Locate platelets.
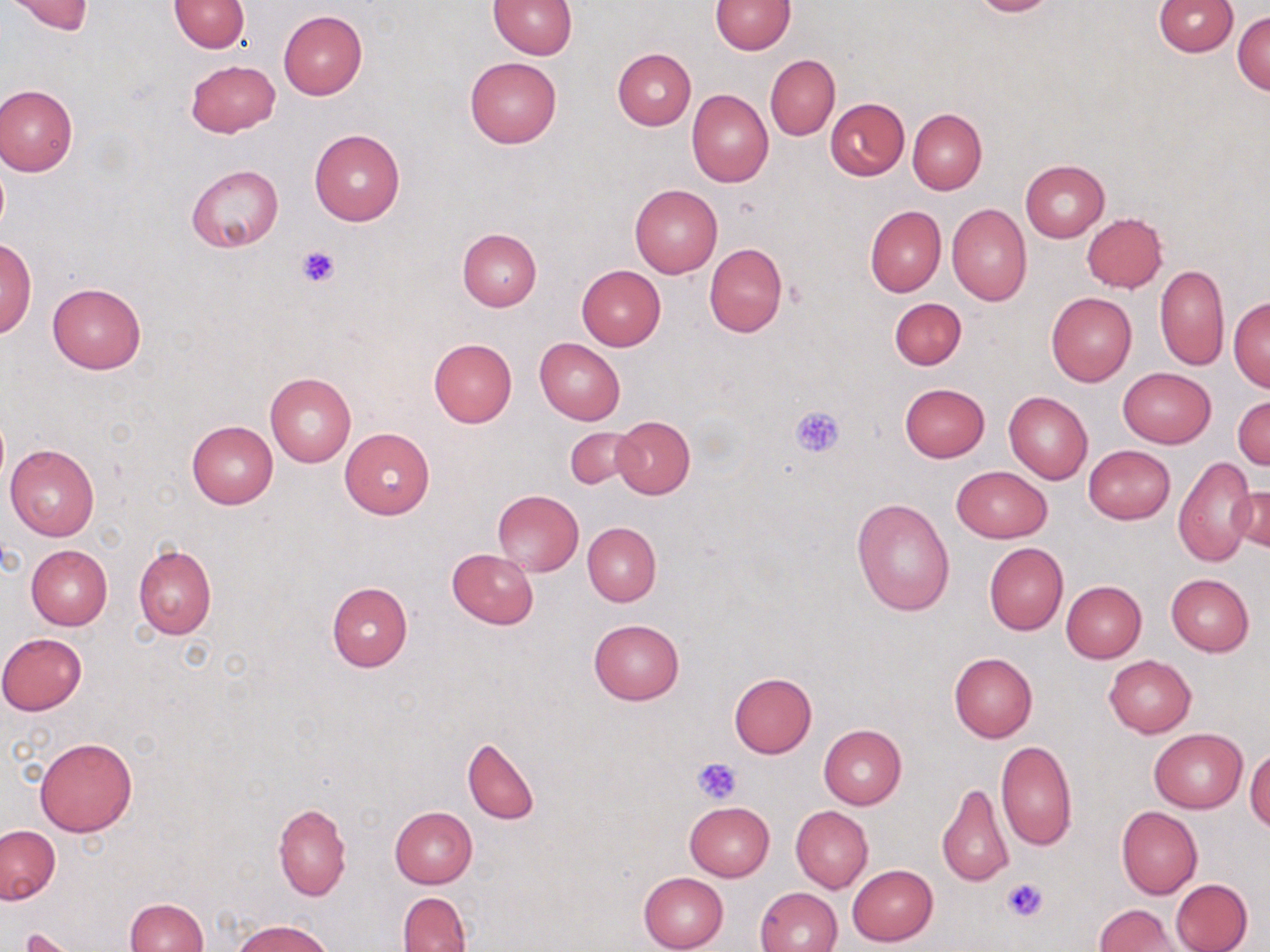
Approximate bounding boxes as named x1/y1/x2/y2 corners in pixels.
Platelets: (x1=295, y1=242, x2=342, y2=287), (x1=790, y1=405, x2=846, y2=457), (x1=691, y1=757, x2=743, y2=803), (x1=1003, y1=876, x2=1051, y2=923), (x1=22, y1=928, x2=80, y2=951).

slide-level diagnosis = negative for blood parasites
image size = 1270×952 pixels
uninfected red blood cell locations = approximate bounding boxes as named x1/y1/x2/y2 corners in pixels: (x1=169, y1=0, x2=250, y2=52), (x1=489, y1=0, x2=576, y2=58), (x1=711, y1=0, x2=795, y2=54), (x1=966, y1=0, x2=1058, y2=17), (x1=1152, y1=0, x2=1238, y2=56), (x1=5, y1=1, x2=94, y2=35), (x1=278, y1=9, x2=367, y2=99), (x1=1233, y1=11, x2=1270, y2=96), (x1=613, y1=49, x2=695, y2=129), (x1=766, y1=54, x2=839, y2=141), (x1=464, y1=55, x2=562, y2=149), (x1=186, y1=59, x2=280, y2=138), (x1=0, y1=84, x2=78, y2=175), (x1=686, y1=89, x2=774, y2=187), (x1=826, y1=98, x2=909, y2=180), (x1=908, y1=109, x2=987, y2=194), (x1=309, y1=129, x2=405, y2=226), (x1=1020, y1=160, x2=1110, y2=242), (x1=187, y1=165, x2=283, y2=253), (x1=629, y1=183, x2=723, y2=278), (x1=946, y1=203, x2=1032, y2=307), (x1=865, y1=205, x2=947, y2=297), (x1=1082, y1=213, x2=1168, y2=292), (x1=457, y1=228, x2=542, y2=312), (x1=1, y1=238, x2=36, y2=339), (x1=704, y1=242, x2=788, y2=337), (x1=1154, y1=264, x2=1228, y2=370), (x1=576, y1=265, x2=666, y2=350), (x1=48, y1=283, x2=146, y2=374), (x1=1046, y1=292, x2=1136, y2=386), (x1=1228, y1=296, x2=1270, y2=390), (x1=889, y1=297, x2=965, y2=370), (x1=428, y1=338, x2=518, y2=429), (x1=534, y1=339, x2=625, y2=425), (x1=1118, y1=367, x2=1216, y2=448), (x1=265, y1=371, x2=357, y2=467), (x1=899, y1=383, x2=989, y2=461), (x1=1004, y1=392, x2=1093, y2=483), (x1=1233, y1=395, x2=1270, y2=471), (x1=613, y1=416, x2=695, y2=498), (x1=187, y1=421, x2=278, y2=508), (x1=565, y1=427, x2=639, y2=490), (x1=340, y1=428, x2=435, y2=519), (x1=5, y1=442, x2=99, y2=542), (x1=1083, y1=444, x2=1176, y2=525), (x1=1173, y1=455, x2=1255, y2=568), (x1=952, y1=466, x2=1051, y2=543), (x1=1230, y1=486, x2=1269, y2=556), (x1=491, y1=490, x2=583, y2=576), (x1=852, y1=498, x2=955, y2=616), (x1=582, y1=523, x2=661, y2=606), (x1=984, y1=543, x2=1068, y2=635), (x1=134, y1=544, x2=216, y2=640), (x1=25, y1=545, x2=112, y2=630), (x1=447, y1=549, x2=539, y2=629), (x1=1166, y1=573, x2=1254, y2=656), (x1=1060, y1=581, x2=1146, y2=663), (x1=327, y1=582, x2=412, y2=672), (x1=589, y1=619, x2=684, y2=705), (x1=1, y1=632, x2=87, y2=715), (x1=948, y1=652, x2=1037, y2=743), (x1=1103, y1=655, x2=1196, y2=737), (x1=729, y1=672, x2=817, y2=759), (x1=818, y1=724, x2=906, y2=810), (x1=1149, y1=727, x2=1248, y2=813), (x1=462, y1=736, x2=538, y2=825), (x1=35, y1=737, x2=137, y2=837), (x1=995, y1=740, x2=1077, y2=851), (x1=1245, y1=747, x2=1270, y2=830), (x1=937, y1=782, x2=1014, y2=889), (x1=685, y1=801, x2=775, y2=880), (x1=273, y1=802, x2=351, y2=901), (x1=790, y1=806, x2=873, y2=893), (x1=1116, y1=806, x2=1203, y2=899), (x1=389, y1=807, x2=477, y2=888), (x1=1, y1=824, x2=60, y2=904), (x1=847, y1=864, x2=937, y2=946), (x1=638, y1=872, x2=729, y2=952), (x1=1170, y1=878, x2=1252, y2=952), (x1=754, y1=887, x2=842, y2=952), (x1=398, y1=891, x2=471, y2=952), (x1=124, y1=898, x2=207, y2=952), (x1=1094, y1=905, x2=1182, y2=951), (x1=232, y1=920, x2=331, y2=952), (x1=19, y1=928, x2=78, y2=952)
preparation = thin blood film
magnification = 1000x
field of view = one of a larger specimen
stain = May-Grünwald-Giemsa
modality = light microscopy